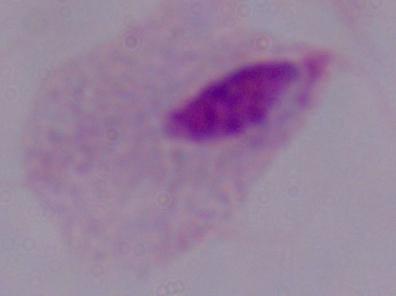
Summary:
  - Magnification: 1000x
  - Modality: photomicrograph
  - Identification: trichomonad